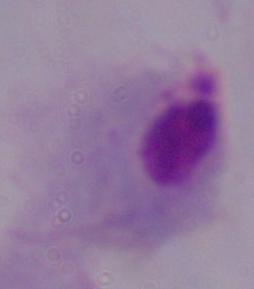

identification: trichomonad
magnification: 1000x
modality: micrograph